Classify this cell by malaria status.
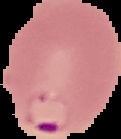
It is parasitized.

image size = 121×139 pixels
image type = cell region segmented out of the field of view; surrounding area masked to black
preparation = thin blood film